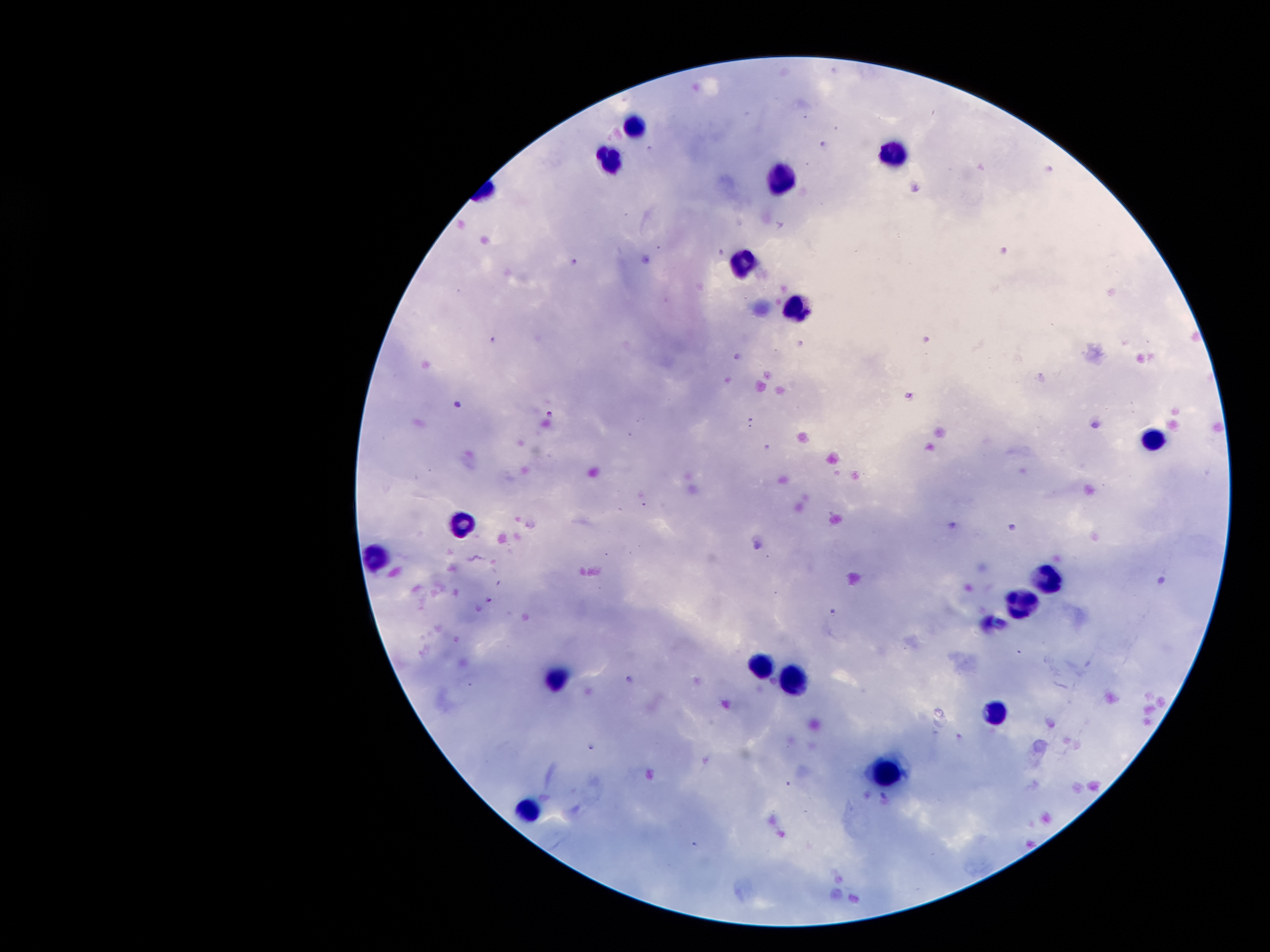

coordinate format = approximate object centers, in pixels from the top-left corner
malaria parasite locations = (x=575, y=263), (x=494, y=340), (x=908, y=395), (x=459, y=407), (x=550, y=414), (x=490, y=599), (x=832, y=612)
leukocyte locations = (x=636, y=121), (x=895, y=150), (x=607, y=158), (x=775, y=178), (x=743, y=264), (x=797, y=309), (x=1152, y=439), (x=461, y=521), (x=373, y=556), (x=1048, y=581), (x=1022, y=598), (x=763, y=666), (x=557, y=677), (x=797, y=681), (x=994, y=713), (x=891, y=773), (x=525, y=813)
preparation = thick blood smear
image size = 1270×952 pixels
capture = smartphone through the microscope eyepiece
magnification = 100x
stain = Giemsa
field of view = one from this slide
patient malaria status = infected with Plasmodium falciparum